Name the parasite shown.
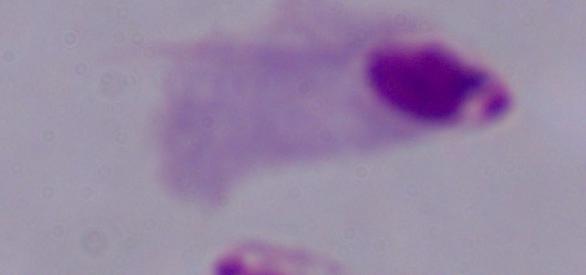

A trichomonad.

Photomicrograph. Captured at 1000x magnification.